Give the extent of all Plasmodium malariae-infected red blood cells.
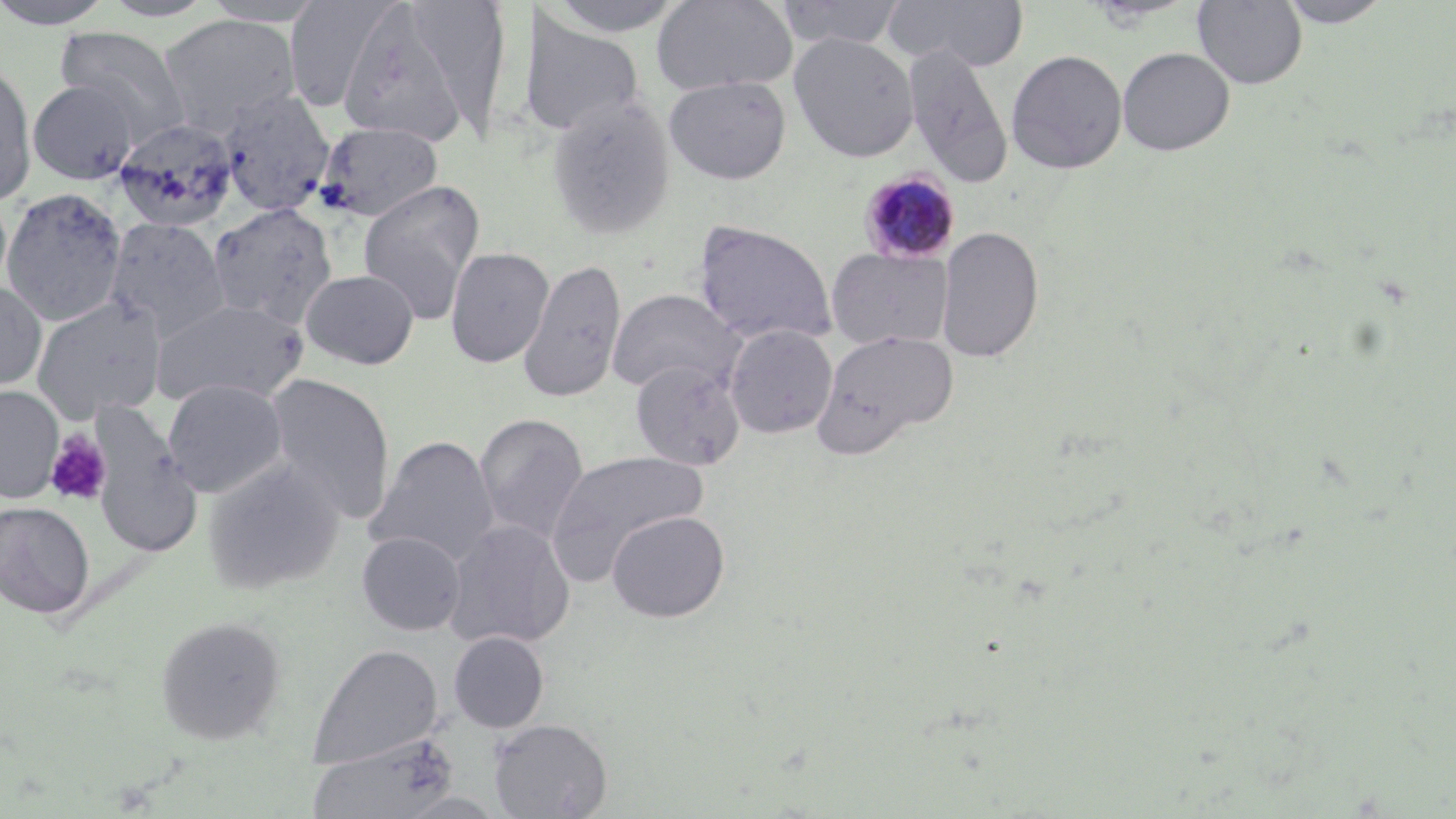

Approximate bounding boxes as named x1/y1/x2/y2 corners in pixels.
Plasmodium malariae-infected red blood cells: (x1=859, y1=170, x2=960, y2=264).

Platelet locations: (x1=44, y1=430, x2=112, y2=506). Uninfected red blood cell locations: (x1=0, y1=0, x2=117, y2=29), (x1=98, y1=0, x2=220, y2=22), (x1=200, y1=0, x2=329, y2=27), (x1=283, y1=0, x2=403, y2=113), (x1=541, y1=0, x2=691, y2=38), (x1=652, y1=0, x2=797, y2=96), (x1=773, y1=0, x2=908, y2=50), (x1=883, y1=0, x2=1029, y2=72), (x1=1192, y1=0, x2=1308, y2=90), (x1=1276, y1=0, x2=1393, y2=28), (x1=398, y1=1, x2=514, y2=135), (x1=336, y1=4, x2=472, y2=147), (x1=518, y1=13, x2=646, y2=138), (x1=157, y1=14, x2=301, y2=135), (x1=55, y1=26, x2=192, y2=145), (x1=789, y1=33, x2=919, y2=162), (x1=902, y1=42, x2=1015, y2=189), (x1=1117, y1=46, x2=1235, y2=157), (x1=1006, y1=49, x2=1127, y2=175), (x1=0, y1=61, x2=36, y2=207), (x1=663, y1=76, x2=791, y2=184), (x1=28, y1=80, x2=138, y2=185), (x1=218, y1=91, x2=336, y2=217), (x1=546, y1=97, x2=676, y2=242), (x1=113, y1=118, x2=239, y2=231), (x1=317, y1=121, x2=445, y2=222), (x1=357, y1=179, x2=486, y2=322), (x1=2, y1=188, x2=127, y2=326), (x1=206, y1=202, x2=337, y2=329), (x1=104, y1=217, x2=231, y2=341), (x1=693, y1=220, x2=837, y2=345), (x1=936, y1=224, x2=1045, y2=364), (x1=445, y1=246, x2=555, y2=368), (x1=826, y1=247, x2=953, y2=350), (x1=517, y1=257, x2=628, y2=404), (x1=300, y1=269, x2=419, y2=369), (x1=0, y1=279, x2=48, y2=392), (x1=606, y1=288, x2=745, y2=397), (x1=31, y1=296, x2=168, y2=423), (x1=151, y1=297, x2=310, y2=408), (x1=723, y1=324, x2=837, y2=438), (x1=812, y1=329, x2=960, y2=456), (x1=630, y1=359, x2=746, y2=471), (x1=265, y1=374, x2=395, y2=522), (x1=162, y1=379, x2=288, y2=498), (x1=0, y1=385, x2=64, y2=503), (x1=474, y1=412, x2=590, y2=544), (x1=92, y1=418, x2=203, y2=560), (x1=365, y1=435, x2=500, y2=568), (x1=545, y1=450, x2=709, y2=580), (x1=202, y1=460, x2=345, y2=595), (x1=0, y1=501, x2=95, y2=619), (x1=606, y1=510, x2=730, y2=622), (x1=443, y1=519, x2=576, y2=649), (x1=357, y1=530, x2=466, y2=636), (x1=155, y1=616, x2=287, y2=745), (x1=448, y1=631, x2=549, y2=733), (x1=309, y1=643, x2=443, y2=771), (x1=488, y1=718, x2=613, y2=818), (x1=307, y1=733, x2=460, y2=818), (x1=391, y1=791, x2=510, y2=818). Slide-level diagnosis: Plasmodium malariae. Light microscopy. Captured at 1000x magnification. Image is 1456×819 pixels. May-Grünwald-Giemsa-stained preparation. Thin blood film. One field of a larger specimen.